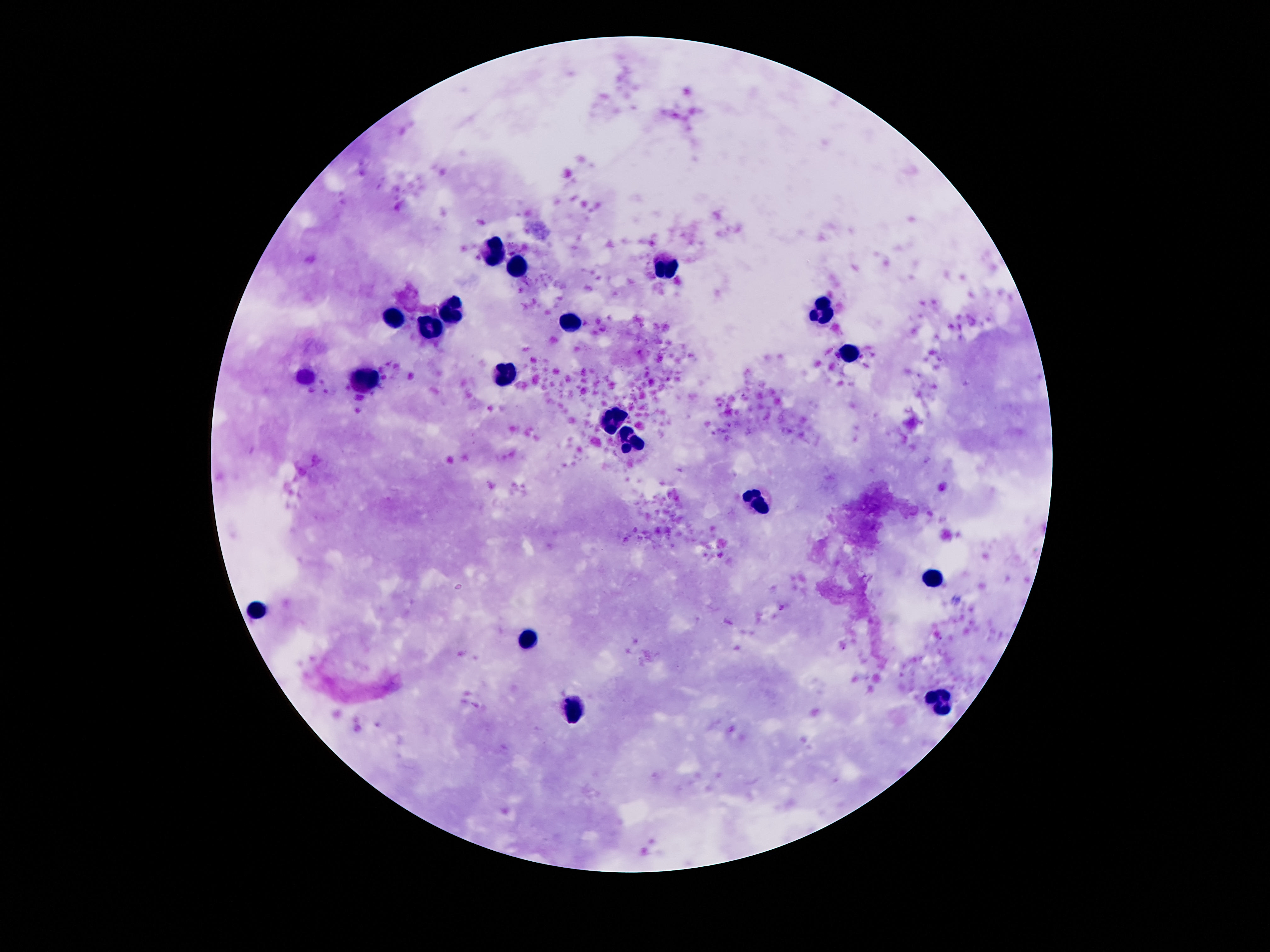
image_size: 1270×952 pixels
leukocyte_locations: 'approximate centers as {x, y} in pixels: {498, 253}, {668, 264}, {518, 266}, {455, 309}, {823, 311}, {391, 320}, {571, 320}, {432, 327}, {850, 355}, {504, 375}, {365, 381}, {612, 422}, {631, 438}, {758, 501}, {932, 581}, {256, 611}, {530, 641}, {940, 704}, {573, 712}'
capture: smartphone camera through the microscope eyepiece
magnification: 100x
patient_malaria_status: not infected
stain: Giemsa
preparation: thick peripheral-blood smear
field_of_view: single